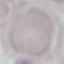
Summary:
  - Result: no malaria parasites seen
  - Image type: cell patch, automatically extracted from a larger field of view and resized to 64 × 64 pixels
  - Preparation: thin blood film
  - Stain: Giemsa
  - Capture: smartphone through the microscope eyepiece